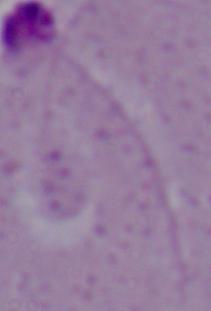 Captured at 1000x magnification. Photomicrograph. A Leishmania parasite is seen.